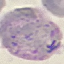

Malaria status: parasitized. Cell patch, automatically extracted from a larger field of view and resized to 64 × 64 pixels. Thin blood smear. Giemsa-stained preparation. Photographed with a smartphone camera at the microscope eyepiece.